Classify this cell by malaria status.
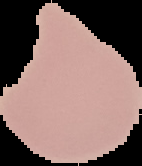

It is uninfected.

Summary:
  - Image type: cell region segmented out of the field of view; surrounding area masked to black
  - Preparation: thin blood film
  - Image size: 142×166 pixels